Comment on the morphology of the red blood cells.
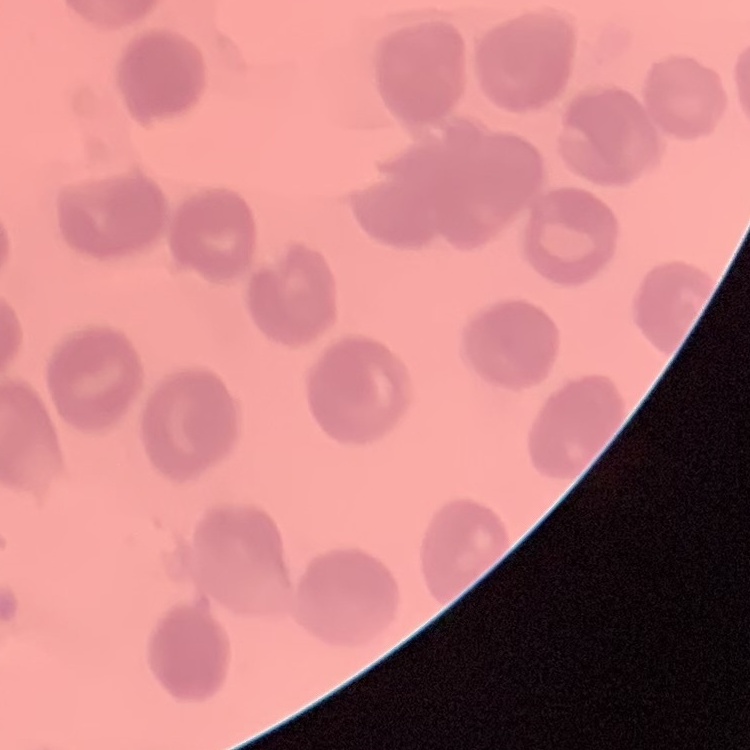

No rouleaux formation.

Square crop of a larger photomicrograph. Field's or Giemsa stain. Thin blood film.